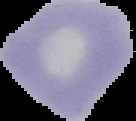

preparation = thin blood film
image size = 136×121 pixels
image type = cell region segmented out of the field of view; surrounding area masked to black
result = no malaria parasites detected